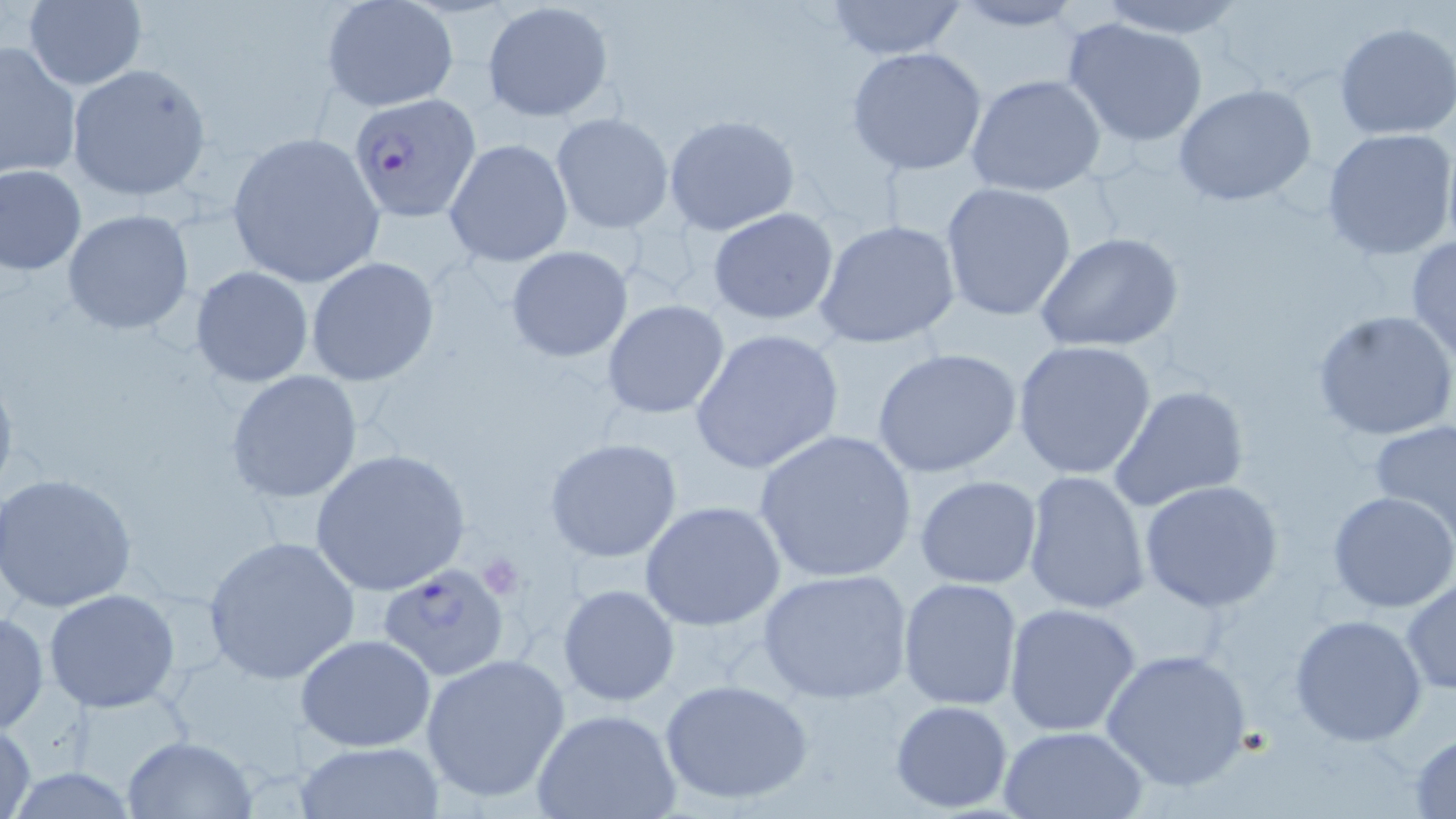
{
  "slide_level_diagnosis": "Plasmodium falciparum",
  "stain": "May-Grünwald-Giemsa",
  "image_size": "1456×819 pixels",
  "magnification": "1000x",
  "platelet_locations": "approximate bounding boxes as (x1, y1, x2, y2) in pixels: (476, 554, 524, 598)",
  "modality": "optical microscopy",
  "field_of_view": "one of a larger specimen",
  "plasmodium_falciparum_infected_red_blood_cell_locations": "approximate bounding boxes as (x1, y1, x2, y2) in pixels: (351, 92, 481, 220), (381, 560, 515, 685)",
  "uninfected_red_blood_cell_locations": "approximate bounding boxes as (x1, y1, x2, y2) in pixels: (822, 0, 971, 60), (945, 0, 1084, 32), (1091, 0, 1253, 37), (21, 1, 148, 89), (320, 1, 460, 113), (481, 1, 613, 121), (1061, 15, 1212, 148), (1334, 22, 1455, 140), (0, 39, 82, 181), (846, 46, 989, 175), (66, 64, 211, 201), (966, 73, 1107, 197), (1173, 84, 1318, 206), (550, 112, 674, 235), (664, 113, 799, 235), (1322, 128, 1456, 261), (227, 133, 383, 286), (444, 137, 574, 268), (1, 164, 87, 275), (939, 182, 1077, 322), (706, 206, 839, 325), (63, 208, 195, 336), (814, 219, 961, 349), (1033, 232, 1185, 353), (1406, 235, 1456, 362), (505, 245, 633, 361), (305, 257, 440, 387), (190, 265, 315, 387), (602, 300, 730, 419), (1312, 309, 1455, 441), (690, 328, 844, 475), (1010, 339, 1158, 481), (872, 347, 1024, 478), (0, 362, 19, 505), (226, 370, 364, 504), (1109, 384, 1249, 512), (1370, 420, 1456, 533), (752, 429, 919, 584), (544, 438, 683, 564), (308, 448, 471, 597), (1021, 469, 1152, 616), (1, 472, 138, 612), (914, 475, 1043, 590), (1139, 480, 1284, 611), (1327, 490, 1456, 612), (639, 499, 785, 633), (202, 535, 360, 684), (757, 567, 916, 706), (897, 577, 1024, 710), (1401, 577, 1456, 695), (558, 583, 679, 708), (43, 589, 183, 714), (1003, 601, 1143, 737), (0, 610, 48, 734), (1289, 613, 1428, 745), (295, 634, 439, 753), (1100, 648, 1253, 794), (420, 652, 573, 804), (659, 677, 814, 807), (888, 699, 1015, 813), (533, 709, 681, 819), (1, 720, 37, 819), (997, 725, 1149, 819), (1407, 733, 1456, 816), (122, 735, 257, 818), (294, 740, 445, 818)",
  "preparation": "thin blood smear"
}